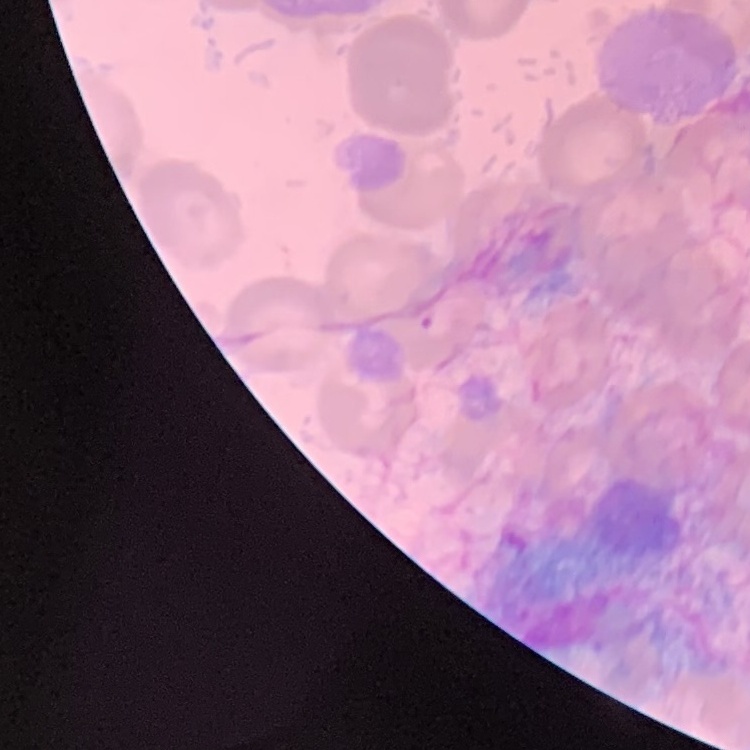 The erythrocytes show no rouleaux formation. Stained with either Field's or Giemsa. Thin peripheral smear. One tile cut from a larger photomicrograph.